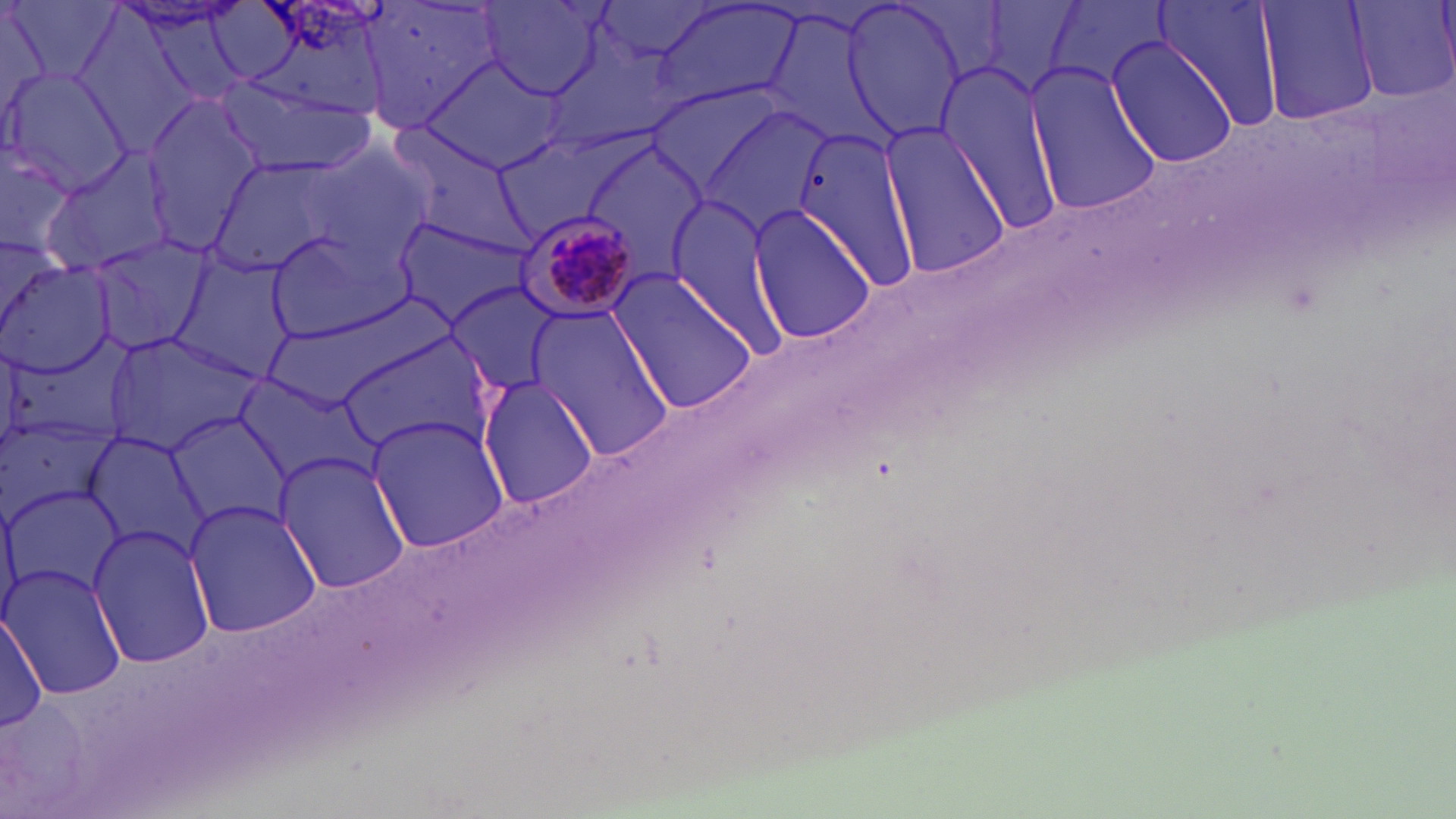

{
  "plasmodium_malariae_infected_red_blood_cell_locations": "approximate bounding boxes as [x1, y1, x2, y2] in pixels: [510, 211, 643, 324]",
  "slide_level_diagnosis": "Plasmodium malariae",
  "field_of_view": "one of a larger specimen",
  "image_size": "1456×819 pixels",
  "magnification": "1000x",
  "stain": "May-Grünwald-Giemsa",
  "modality": "optical microscopy",
  "preparation": "thin blood film",
  "uninfected_red_blood_cell_locations": "approximate bounding boxes as [x1, y1, x2, y2] in pixels: [248, 0, 395, 120], [358, 0, 505, 133], [1153, 0, 1285, 127], [1257, 0, 1381, 124], [8, 1, 120, 89], [979, 1, 1087, 95], [1046, 1, 1170, 91], [1351, 1, 1454, 103], [839, 2, 967, 140], [478, 3, 608, 98], [652, 3, 800, 112], [1, 6, 49, 135], [761, 7, 896, 148], [1105, 38, 1240, 170], [420, 56, 564, 172], [935, 64, 1063, 233], [1025, 65, 1162, 215], [2, 67, 130, 194], [215, 75, 369, 178], [644, 82, 788, 198], [142, 98, 260, 253], [697, 103, 833, 238], [390, 125, 528, 250], [793, 126, 920, 291], [881, 126, 1011, 279], [492, 137, 614, 236], [304, 141, 435, 268], [577, 142, 708, 281], [0, 143, 78, 262], [40, 149, 174, 276], [204, 156, 351, 281], [665, 199, 793, 360], [746, 202, 878, 345], [394, 216, 534, 326], [264, 230, 407, 340], [86, 236, 214, 355], [173, 256, 296, 383], [1, 262, 116, 380], [611, 272, 756, 414], [448, 281, 557, 392], [526, 306, 672, 458], [0, 332, 133, 454], [103, 332, 261, 453], [335, 333, 497, 458], [228, 372, 379, 489], [479, 376, 599, 508], [168, 411, 291, 531], [0, 412, 118, 523], [368, 416, 510, 554], [78, 429, 212, 560], [273, 451, 409, 595], [1, 484, 126, 600], [184, 500, 321, 637], [87, 523, 217, 669], [3, 566, 126, 699], [1, 613, 48, 732]"
}